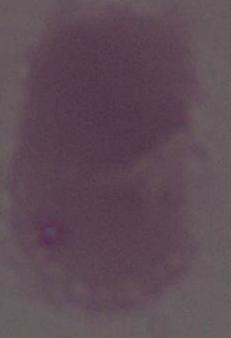
modality: micrograph
magnification: 1000x
identification: erythrocyte